State the preparation type.
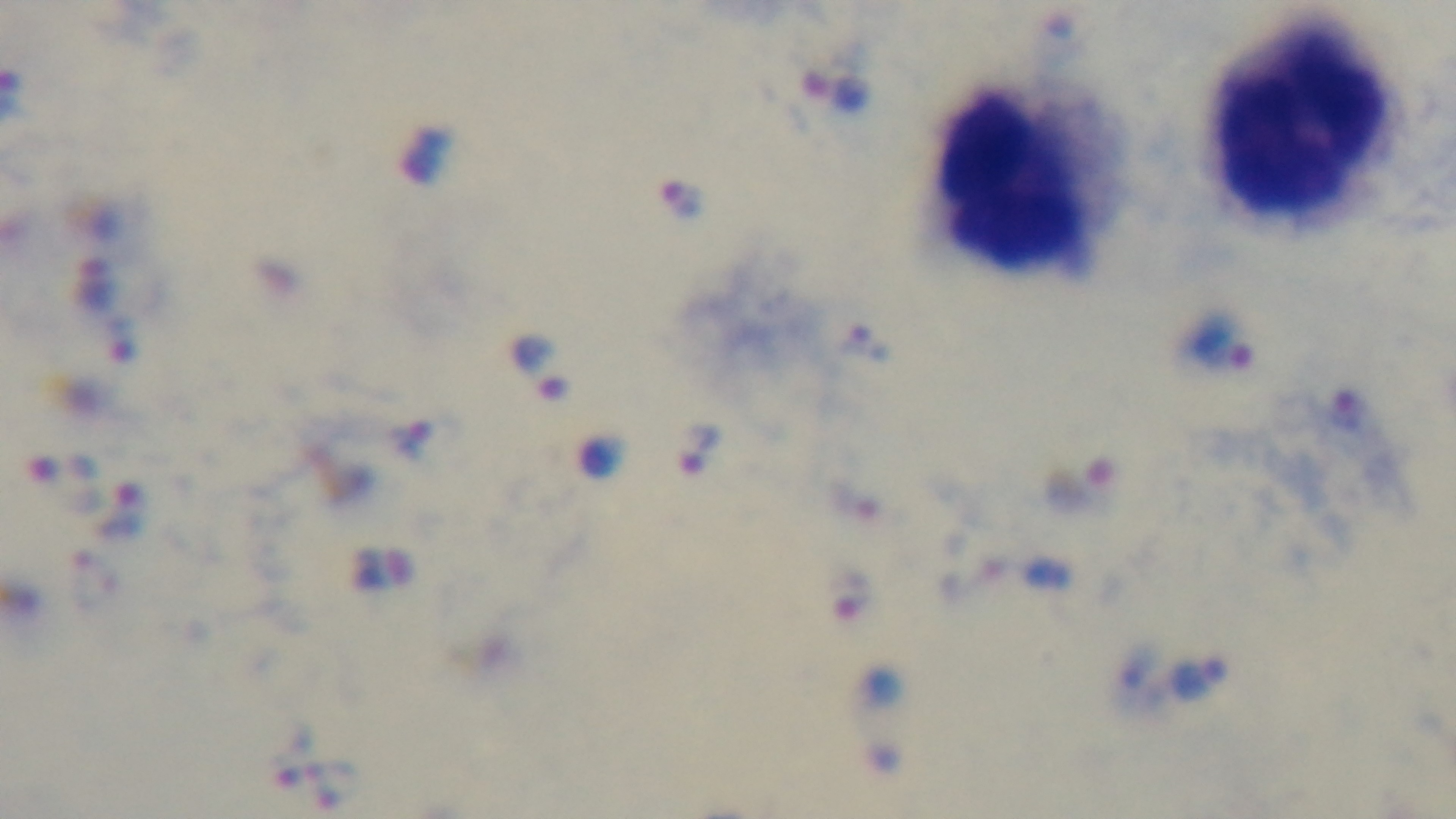

It is a thick blood film.

Giemsa-stained. Captured with a mounted 4K digital camera. Single field of view. Photomicrograph. Malaria status: positive. Oil-immersion objective, 100x.